State which parasite is depicted.
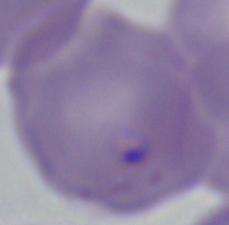
This is Babesia.

Summary:
  - Modality: micrograph
  - Magnification: 1000x